Assess this cell for malaria.
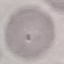
It is uninfected.

Summary:
  - Image type: automatically extracted cell patch, resized to 64 × 64 pixels
  - Capture: smartphone through the microscope eyepiece
  - Preparation: thin blood smear
  - Stain: Giemsa